Report the malaria status of this cell.
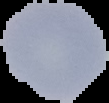

Uninfected.

Summary:
  - Image size: 109×103 pixels
  - Preparation: thin blood smear
  - Image type: segmented cell region with the area outside set to black